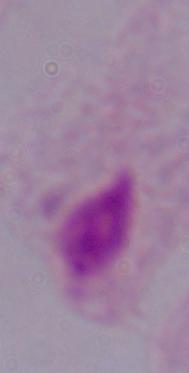
Captured at 1000x magnification. A trichomonad is shown. Photomicrograph.